Identify the preparation type.
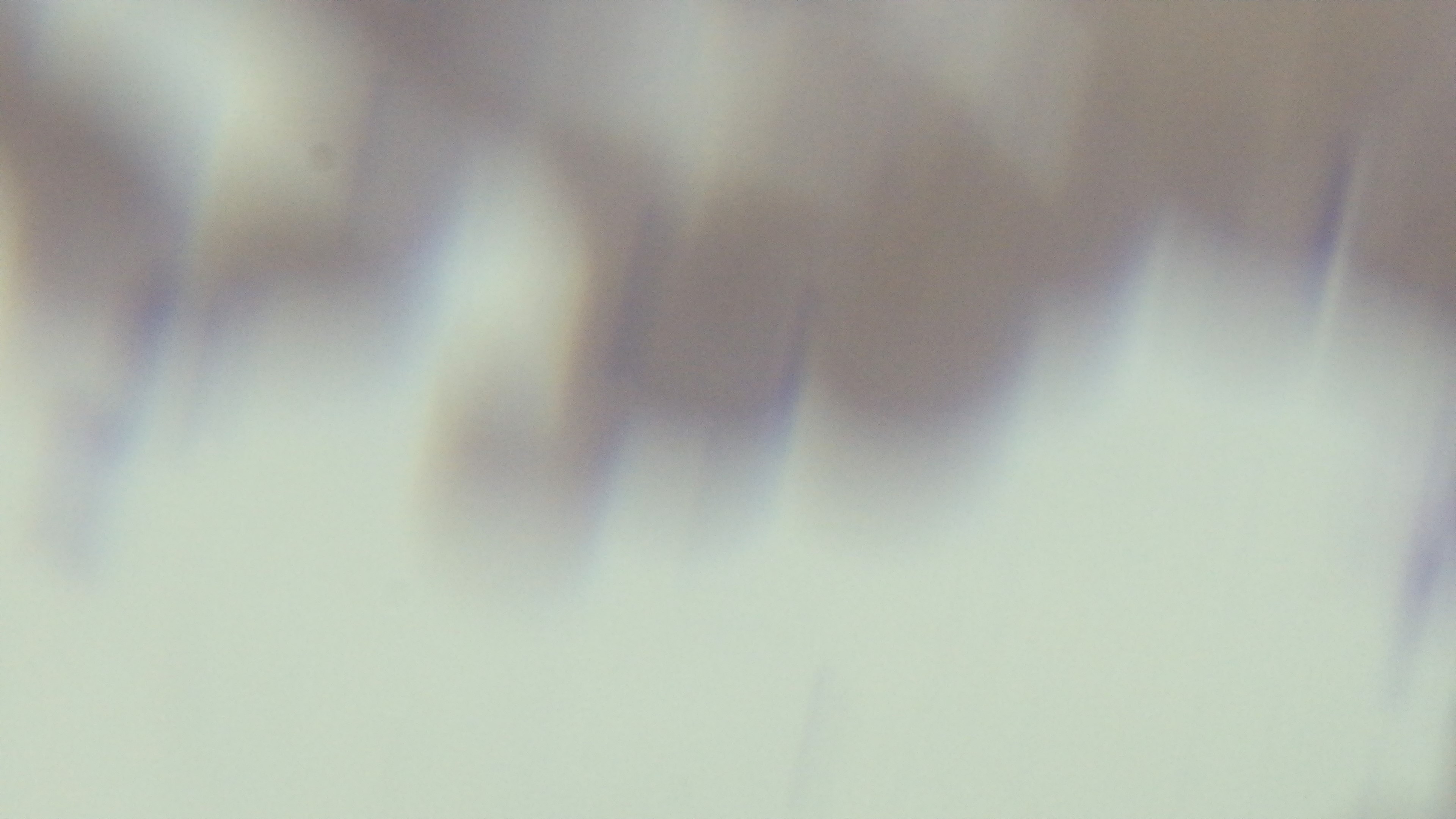
Thin.

Single field of view. Captured with a mounted 4K digital camera. Giemsa-stained. 100x oil-immersion objective. Malaria status: positive. Photomicrograph.